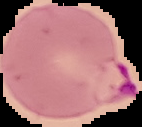
{
  "image_size": "142×127 pixels",
  "image_type": "segmented cell region on a black background",
  "preparation": "thin blood film",
  "malaria_status": "parasitized"
}